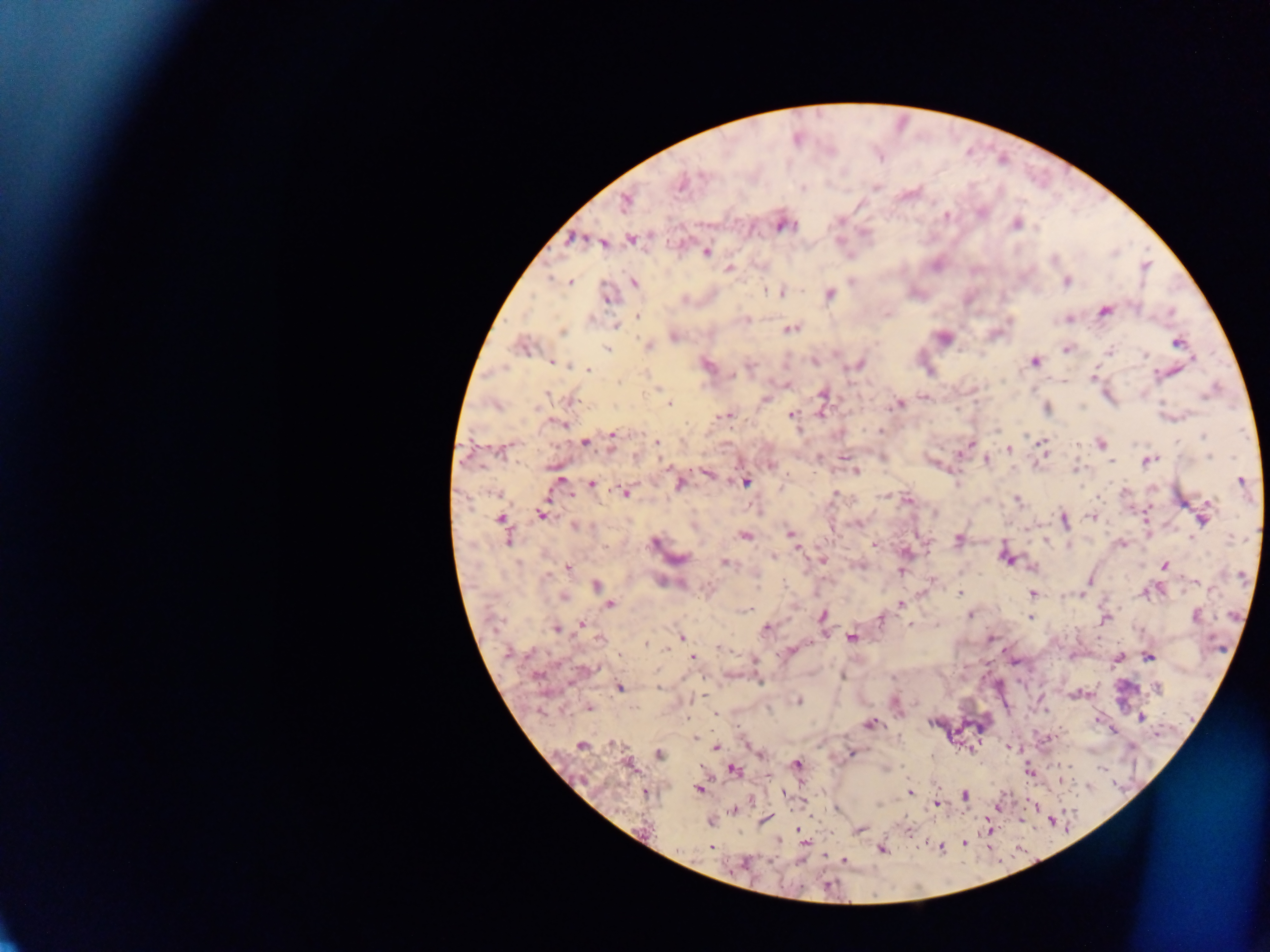

{
  "capture": "mobile-phone photograph through a microscope",
  "country": "Ghana",
  "plasmodium_parasite_locations": "approximate centers as [x, y] in pixels: [680, 183], [625, 201], [980, 212], [946, 215], [783, 224], [1016, 224], [575, 238], [632, 240], [602, 241], [705, 252], [1145, 266], [728, 269], [570, 281], [1066, 281], [633, 283], [781, 292], [829, 293], [607, 298], [1103, 311], [638, 316], [1067, 318], [745, 319], [1010, 321], [616, 325], [790, 329], [561, 332], [673, 336], [943, 337], [1177, 342], [522, 345], [647, 345], [606, 348], [1067, 348], [1108, 350], [813, 360], [551, 362], [1034, 362], [705, 364], [858, 364], [588, 369], [1172, 370], [1092, 375], [787, 384], [659, 389], [546, 394], [823, 394], [1107, 394], [923, 396], [570, 400], [765, 400], [668, 403], [897, 404], [1046, 408], [726, 415], [792, 415], [557, 421], [879, 430], [613, 434], [583, 442], [611, 442], [656, 442], [1041, 443], [1099, 443], [970, 444], [502, 449], [1009, 449], [1042, 451], [986, 459], [1147, 459], [771, 465], [855, 470], [707, 473], [560, 481], [1241, 481], [678, 482], [745, 482], [591, 484], [624, 492], [836, 495], [885, 497], [907, 499], [1018, 500], [541, 514], [1145, 514], [1091, 517], [1203, 517], [501, 518], [1064, 520], [857, 523], [574, 526], [693, 526], [789, 534], [744, 535], [508, 537], [957, 539], [1045, 540], [654, 543], [874, 544], [1069, 544], [1122, 544], [797, 547], [905, 552], [773, 556], [1007, 557], [677, 559], [823, 560], [726, 562], [857, 564], [1164, 565], [568, 567], [901, 570], [546, 575], [1195, 582], [596, 586], [959, 593], [1032, 594], [1082, 594], [563, 596], [608, 604], [901, 604], [969, 614], [1195, 615], [822, 616], [1104, 617], [881, 618], [1030, 618], [581, 624], [909, 624], [766, 627], [556, 628], [681, 636], [851, 637], [600, 638], [989, 638], [646, 645], [720, 647], [790, 650], [508, 652], [693, 656], [1148, 656], [1117, 658], [754, 660], [843, 676], [618, 686], [659, 687], [1156, 688], [1076, 694], [798, 700], [895, 701], [588, 707], [715, 713], [1098, 717], [1140, 717], [932, 721], [869, 723], [1113, 730], [1050, 737], [695, 738], [614, 743], [747, 743], [581, 744], [1008, 746], [716, 747], [851, 752], [659, 754], [760, 754], [628, 764], [795, 764], [733, 770], [1029, 771], [1059, 780], [699, 789], [646, 791], [909, 792], [782, 793], [964, 795], [936, 803], [1032, 805], [837, 807], [733, 809], [1020, 819], [764, 820], [1052, 820], [711, 821], [797, 828], [858, 829], [906, 829], [805, 843], [964, 843], [710, 846], [940, 846], [883, 849], [844, 861]",
  "field_of_view": "single",
  "image_size": "1270×952 pixels",
  "preparation": "thick blood film"
}